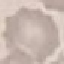
Summary:
  - Result: no malaria parasites detected
  - Image type: automatically extracted cell patch, resized to 64 × 64 pixels
  - Preparation: thin blood smear
  - Stain: Giemsa
  - Capture: smartphone camera at the microscope eyepiece